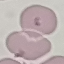 Malaria status: uninfected. Giemsa stain. Photographed with a smartphone camera at the microscope eyepiece. Thin blood smear. Automatically extracted cell patch, resized to 64 × 64 pixels.